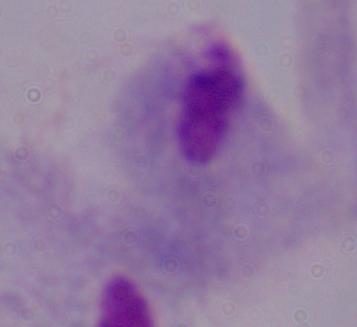

Summary:
  - Modality: photomicrograph
  - Identification: trichomonad
  - Magnification: 1000x